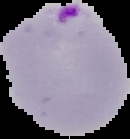
Summary:
  - Image size: 130×139 pixels
  - Preparation: thin blood smear
  - Malaria status: parasitized
  - Image type: segmented cell region with the area outside set to black